State which parasite is depicted.
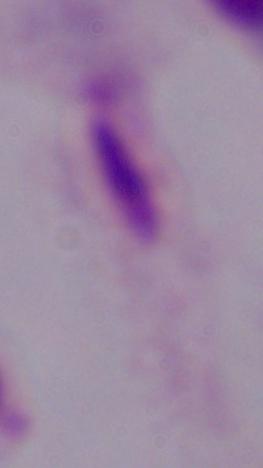
This is a trichomonad.

Micrograph. Captured at 1000x magnification.